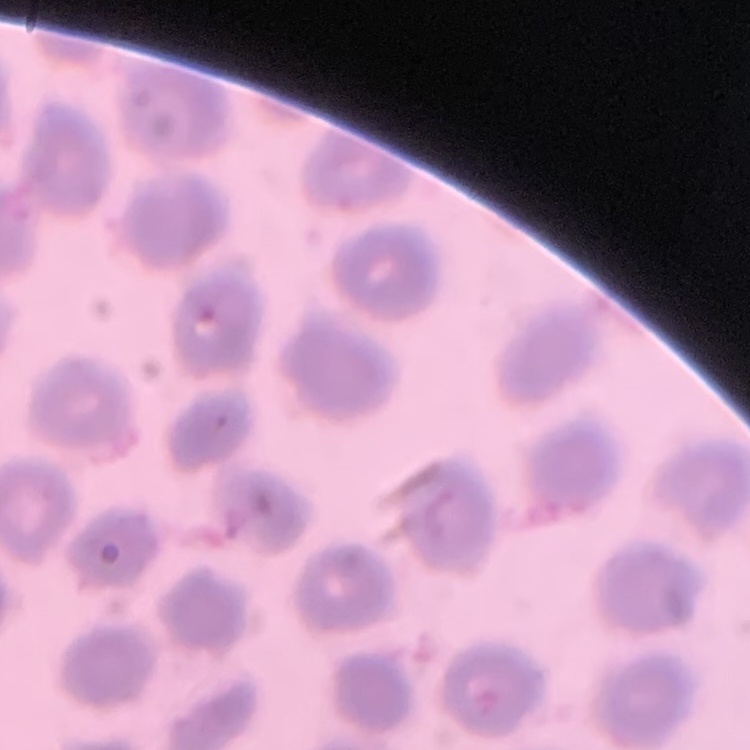

red blood cell morphology = no rouleaux formation
stain = Field's or Giemsa
preparation = thin blood smear
image type = one tile cut from a larger photomicrograph